Classify this cell by malaria status.
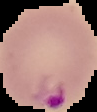
Parasitized.

image size = 97×112 pixels
preparation = thin blood film
image type = segmented cell region with the area outside set to black